Name the parasite shown.
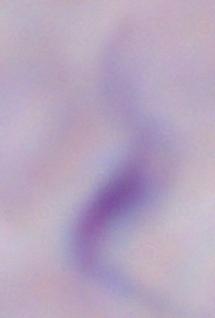

This is a trypanosome.

Photomicrograph. Captured at 1000x magnification.